Classify this cell by malaria status.
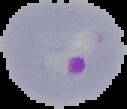
It is parasitized.

Summary:
  - Preparation: thin blood smear
  - Image type: cell region segmented out of the field of view; surrounding area masked to black
  - Image size: 127×109 pixels